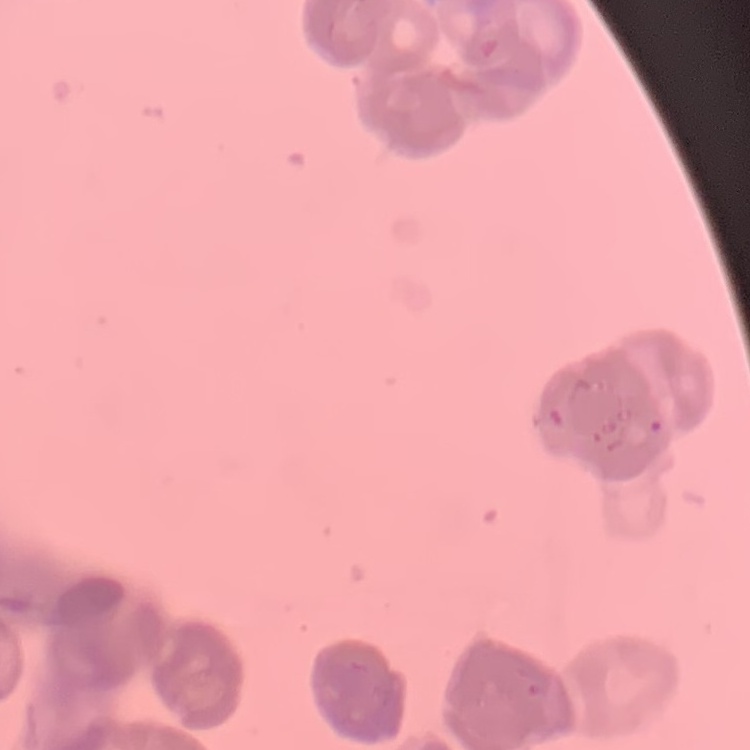

red blood cell morphology = rouleaux formation
image type = one tile cut from a larger photomicrograph
preparation = thin peripheral smear
stain = Field's or Giemsa